Give the position of every leukocyte visible.
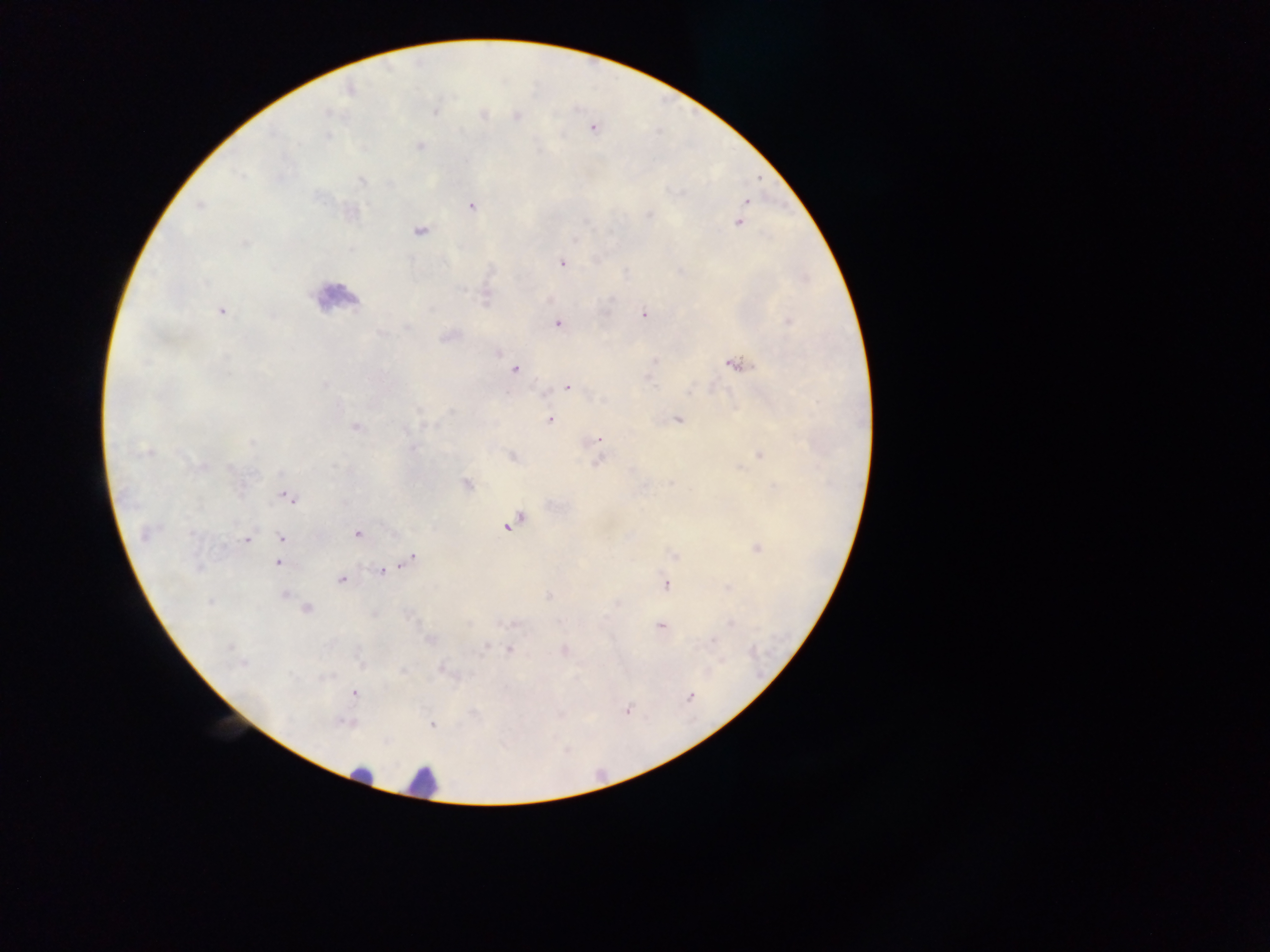
Approximate centers as {x, y} in pixels.
Leukocytes: {358, 777}, {421, 781}.

Malaria parasite locations: {361, 181}, {746, 201}, {200, 206}, {472, 206}, {649, 214}, {738, 223}, {419, 230}, {561, 263}, {221, 311}, {644, 314}, {789, 322}, {558, 324}, {737, 366}, {514, 370}, {567, 388}, {550, 420}, {678, 420}, {598, 438}, {759, 454}, {467, 484}, {287, 497}, {513, 523}, {358, 533}, {144, 534}, {280, 537}, {246, 540}, {757, 547}, {674, 556}, {411, 560}, {278, 563}, {383, 572}, {342, 580}, {665, 584}, {306, 608}, {661, 626}, {713, 641}, {354, 693}, {690, 696}. Collected in Ghana. Mobile-phone photograph taken through the microscope. One field of view. Image is 1270×952 pixels. Thick blood film.